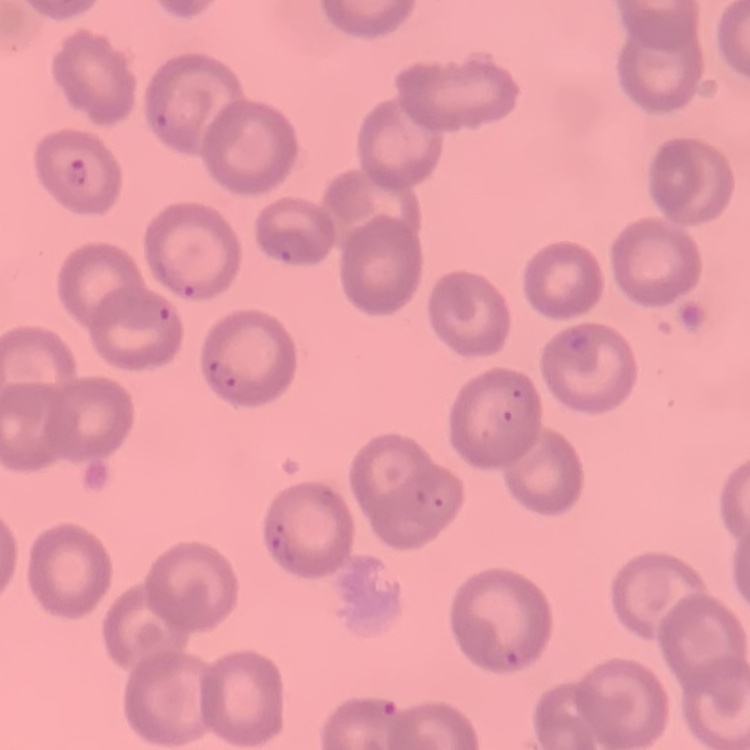
red blood cell morphology = no rouleaux formation
preparation = thin blood smear
image type = square crop of a larger photomicrograph
stain = Field's or Giemsa